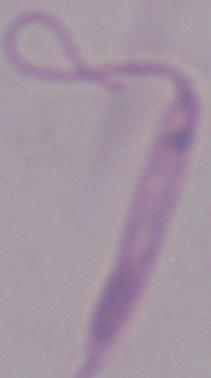

{
  "magnification": "1000x",
  "modality": "photomicrograph",
  "identification": "Leishmania"
}